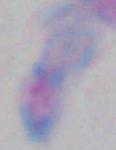
Summary:
  - Identification: Toxoplasma gondii
  - Magnification: 1000x
  - Modality: micrograph